Identify the blood parasite species.
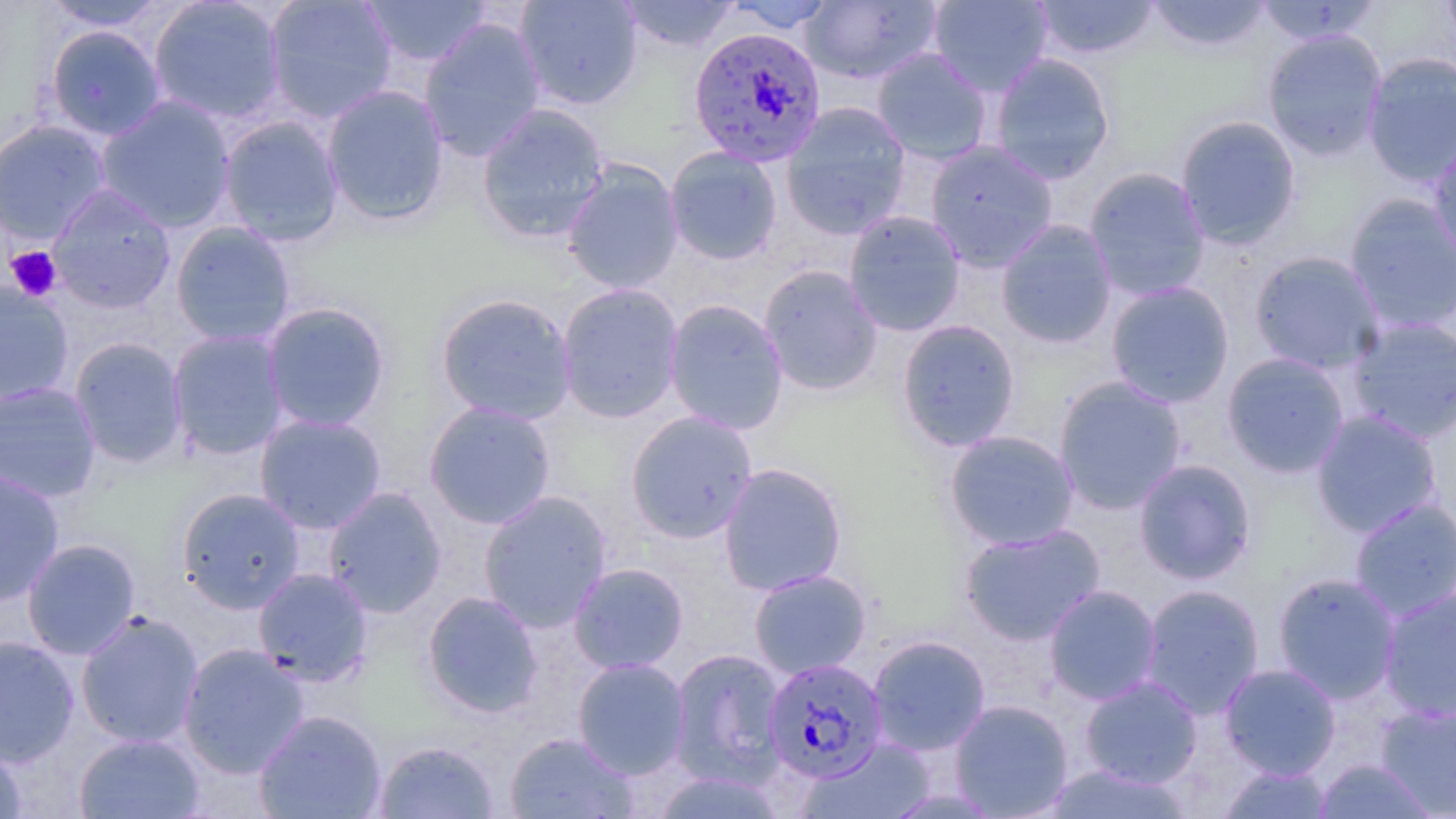

Plasmodium falciparum.

Approximate bounding boxes as (x1,y1)-(x2,y2) corner pairs in pixels. Uninfected red blood cell locations: (43,0)-(169,32), (148,0)-(287,125), (263,0)-(398,123), (514,0)-(644,110), (617,0)-(741,52), (724,0)-(837,33), (800,0)-(941,84), (928,0)-(1052,97), (1032,0)-(1160,59), (1145,0)-(1274,54), (1440,0)-(1456,57), (358,1)-(492,67), (1254,1)-(1382,46), (419,17)-(546,162), (44,24)-(167,141), (1262,29)-(1387,161), (872,48)-(992,165), (990,53)-(1115,185), (1362,53)-(1456,189), (322,84)-(450,227), (95,96)-(236,233), (781,101)-(911,239), (476,103)-(610,245), (218,115)-(344,246), (1175,115)-(1301,249), (0,119)-(112,244), (1428,135)-(1456,266), (925,140)-(1058,272), (665,146)-(782,265), (562,161)-(684,294), (1083,166)-(1211,301), (48,185)-(176,312), (1343,192)-(1456,333), (844,210)-(966,336), (996,219)-(1117,348), (170,221)-(296,348), (1248,250)-(1386,374), (758,265)-(883,396), (0,281)-(74,407), (1106,281)-(1235,408), (557,283)-(685,423), (435,292)-(577,425), (664,299)-(789,435), (261,301)-(392,433), (1345,315)-(1456,444), (896,319)-(1021,452), (167,329)-(290,461), (69,337)-(188,468), (1222,353)-(1350,478), (1054,376)-(1187,515), (0,381)-(102,502), (424,401)-(557,529), (1311,409)-(1443,538), (624,410)-(758,544), (254,413)-(387,534), (943,429)-(1080,551), (1133,458)-(1256,585), (718,462)-(848,596), (0,468)-(65,607), (175,487)-(306,613), (322,487)-(448,618), (478,490)-(612,632), (1349,497)-(1456,622), (959,523)-(1106,646), (21,538)-(141,660), (569,562)-(689,674), (253,567)-(374,686), (748,568)-(872,679), (1272,572)-(1401,703), (1139,583)-(1265,719), (1043,584)-(1163,705), (1379,587)-(1456,721), (422,591)-(544,718), (76,610)-(204,748), (867,635)-(990,756), (0,636)-(80,767), (178,643)-(309,778), (669,648)-(788,785), (572,658)-(691,779), (1219,663)-(1341,780), (1079,675)-(1203,789), (950,699)-(1074,818), (1376,703)-(1456,816), (253,709)-(388,818), (74,732)-(205,818), (504,732)-(637,818), (807,739)-(938,818), (374,740)-(499,818), (0,742)-(28,819), (1316,759)-(1436,818), (1040,762)-(1196,817), (1217,764)-(1334,818). Plasmodium falciparum-infected red blood cell locations: (687,26)-(827,166), (764,658)-(888,784). Platelet locations: (6,246)-(63,302). Thin blood film. Single field of view. May-Grünwald-Giemsa stain. Image is 1456×819 pixels. Captured at 1000x magnification. Light microscopy.